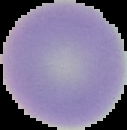
Summary:
  - Image size: 127×130 pixels
  - Preparation: thin blood smear
  - Malaria status: uninfected
  - Image type: segmented cell region on a black background